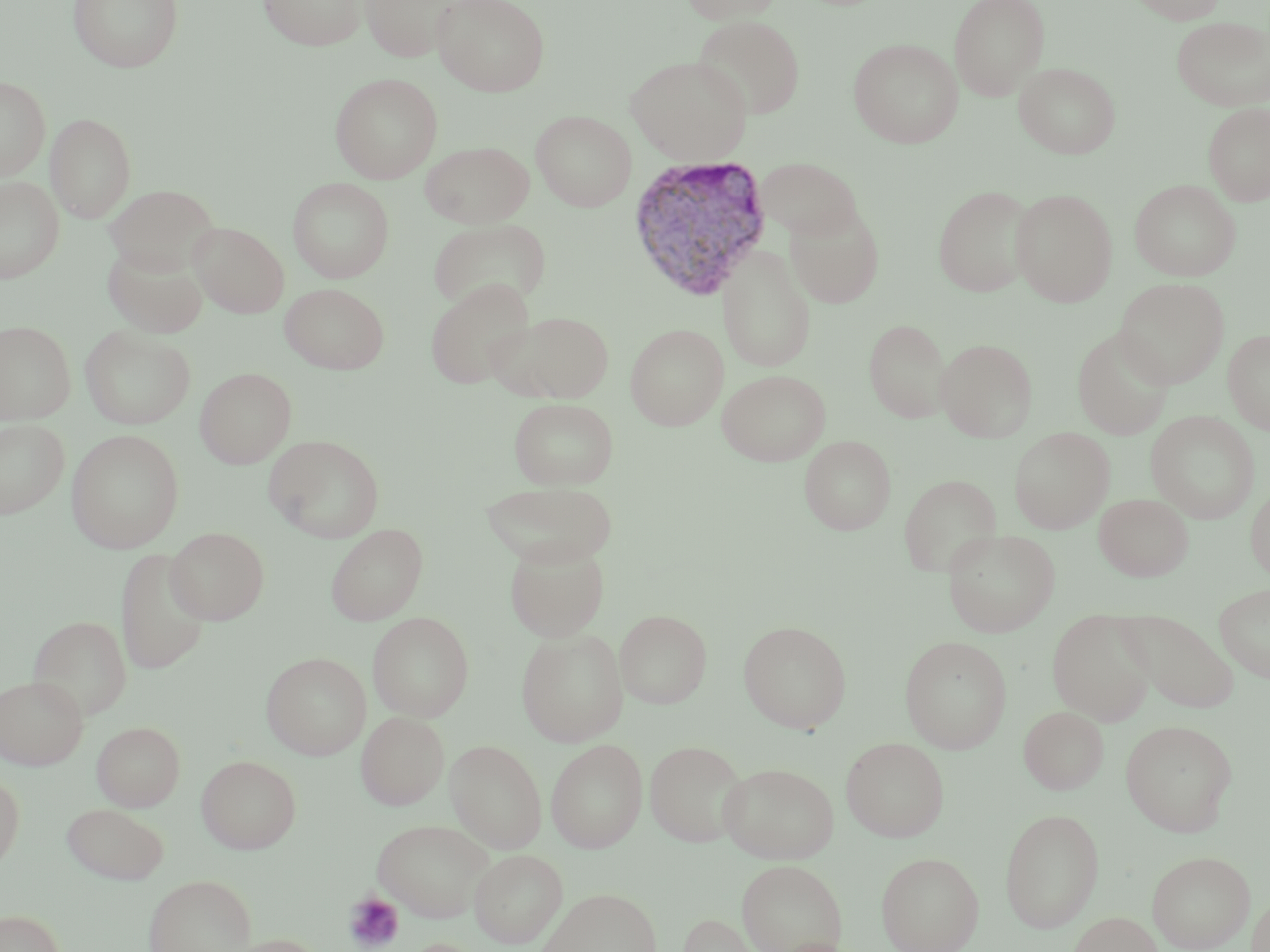
Approximate bounding boxes as (x1,y1)-(x2,y2) corner pairs in pixels. Uninfected red blood cell locations: (69,0)-(183,73), (259,0)-(367,50), (361,0)-(459,62), (432,0)-(550,96), (679,0)-(786,24), (949,0)-(1050,100), (1126,0)-(1229,24), (693,15)-(806,119), (1170,15)-(1270,111), (848,38)-(963,148), (625,55)-(752,164), (1014,61)-(1121,158), (330,72)-(443,183), (0,76)-(50,180), (1203,102)-(1270,206), (531,110)-(636,211), (45,113)-(136,223), (420,141)-(534,228), (755,156)-(864,243), (0,176)-(64,283), (288,178)-(394,283), (1130,179)-(1240,281), (106,184)-(219,273), (933,185)-(1036,297), (1010,189)-(1118,307), (785,204)-(885,308), (428,217)-(551,314), (190,222)-(289,318), (102,243)-(208,338), (718,245)-(817,374), (424,278)-(536,390), (1113,278)-(1229,388), (280,282)-(389,374), (495,310)-(615,403), (864,319)-(952,423), (0,321)-(76,423), (625,323)-(728,430), (80,325)-(195,429), (1072,328)-(1175,440), (1223,329)-(1270,434), (935,338)-(1038,442), (195,368)-(296,468), (717,370)-(831,466), (509,398)-(618,490), (1146,411)-(1260,524), (0,419)-(69,519), (1009,427)-(1114,533), (66,429)-(184,553), (264,435)-(384,543), (799,435)-(896,535), (899,474)-(1001,578), (481,481)-(618,566), (1246,483)-(1270,583), (1094,493)-(1192,581), (325,523)-(428,625), (166,527)-(269,624), (942,528)-(1060,637), (504,541)-(609,641), (115,548)-(211,676), (1214,582)-(1270,683), (615,609)-(712,709), (1047,610)-(1156,726), (1120,610)-(1240,714), (367,612)-(475,721), (27,615)-(132,720), (738,620)-(852,733), (516,628)-(628,746), (899,635)-(1013,754), (261,652)-(371,760), (0,675)-(88,770), (1019,705)-(1109,795), (356,711)-(449,810), (1120,719)-(1238,836), (91,721)-(185,811), (841,737)-(950,842), (445,739)-(547,854), (546,739)-(648,853), (645,741)-(747,846), (197,754)-(302,853), (719,762)-(838,863), (0,772)-(24,875), (62,802)-(170,884), (999,808)-(1105,932), (371,817)-(495,922), (470,849)-(567,948), (1147,850)-(1255,952), (876,851)-(984,952), (736,858)-(847,952), (143,873)-(256,952), (534,887)-(662,952), (1248,890)-(1270,951), (0,909)-(66,952), (677,912)-(773,952), (1066,912)-(1164,952), (217,934)-(330,952). Platelet locations: (344,891)-(404,951). Plasmodium vivax-infected red blood cell locations: (629,154)-(776,301). Slide-level diagnosis: Plasmodium vivax. Captured at 1000x magnification. May-Grünwald-Giemsa stain. Light microscopy. Thin blood smear. One field of a larger specimen. Image is 1270×952 pixels.